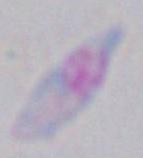
magnification = 1000x
modality = photomicrograph
identification = Toxoplasma gondii